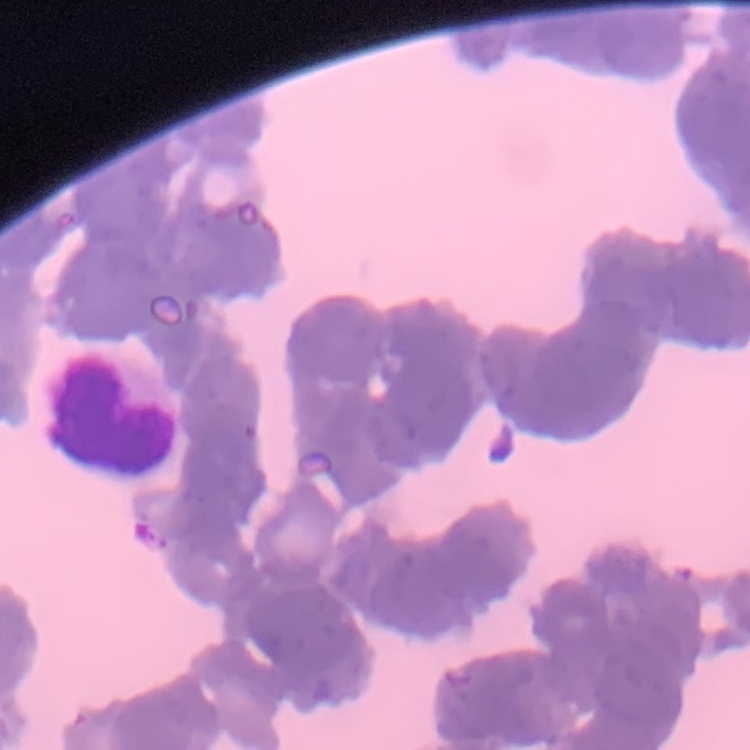
Summary:
  - Red blood cell morphology: rouleaux formation
  - Stain: Field's or Giemsa
  - Preparation: thin blood smear
  - Image type: one tile cut from a larger photomicrograph